Outline each blood parasite and name the species.
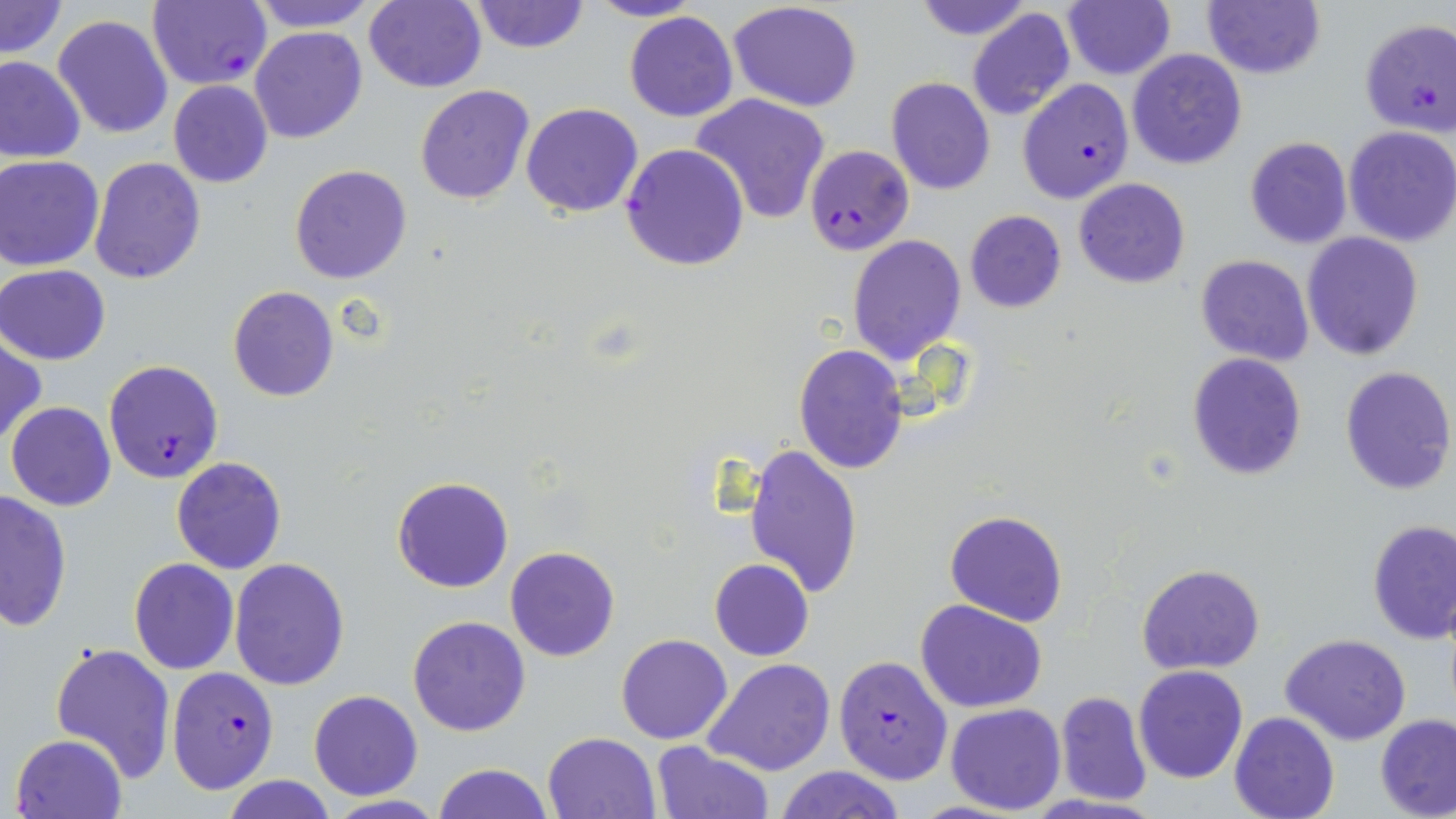
Approximate bounding boxes as (x1,y1)-(x2,y2) corner pairs in pixels.
Plasmodium falciparum-infected red blood cells: (146,0)-(272,90), (1361,19)-(1456,135), (1018,78)-(1134,203), (621,143)-(749,270), (805,144)-(914,257), (105,359)-(223,484), (833,655)-(954,784), (166,666)-(278,793).
No Plasmodium ovale, Plasmodium malariae, Plasmodium vivax, Babesia divergens, or Trypanosoma brucei observed.

Summary:
  - Uninfected red blood cell locations: (0,0)-(68,59), (246,0)-(381,32), (364,0)-(486,93), (467,0)-(590,53), (586,0)-(703,23), (911,0)-(1035,41), (1062,0)-(1176,81), (1202,0)-(1325,79), (726,3)-(863,113), (966,7)-(1076,120), (624,11)-(738,122), (53,14)-(174,140), (250,26)-(367,143), (1127,48)-(1248,169), (0,56)-(85,164), (885,77)-(995,196), (167,80)-(273,188), (415,83)-(536,205), (690,93)-(832,224), (520,103)-(644,217), (1343,127)-(1456,247), (1244,136)-(1352,250), (89,155)-(204,285), (0,156)-(105,271), (289,165)-(412,284), (1074,177)-(1190,288), (965,210)-(1065,313), (1300,231)-(1425,359), (847,234)-(966,364), (1195,255)-(1313,367), (0,264)-(111,365), (227,286)-(339,402), (0,338)-(45,446), (793,344)-(908,474), (1187,352)-(1307,480), (1338,366)-(1455,496), (5,401)-(117,511), (743,443)-(864,600), (171,456)-(287,574), (390,475)-(514,593), (0,489)-(72,633), (944,510)-(1068,627), (1366,519)-(1456,643), (504,546)-(621,662), (228,557)-(350,691), (709,557)-(814,660), (130,558)-(239,675), (1137,565)-(1264,675), (915,600)-(1049,714), (406,616)-(530,737), (616,634)-(733,745), (1282,634)-(1411,744), (49,641)-(176,783), (705,658)-(836,774), (1134,665)-(1249,783), (308,690)-(423,800), (1053,691)-(1153,805), (946,702)-(1066,815), (1229,711)-(1340,819), (1375,714)-(1456,818), (543,731)-(660,817), (10,733)-(128,819), (653,740)-(773,818), (431,762)-(553,819), (775,764)-(905,819), (221,776)-(339,818), (317,795)-(450,818)
  - Slide-level diagnosis: Plasmodium falciparum
  - Preparation: thin blood smear
  - Magnification: 1000x
  - Field of view: single
  - Image size: 1456×819 pixels
  - Stain: May-Grünwald-Giemsa
  - Modality: light microscopy